Describe the morphology of the red blood cells.
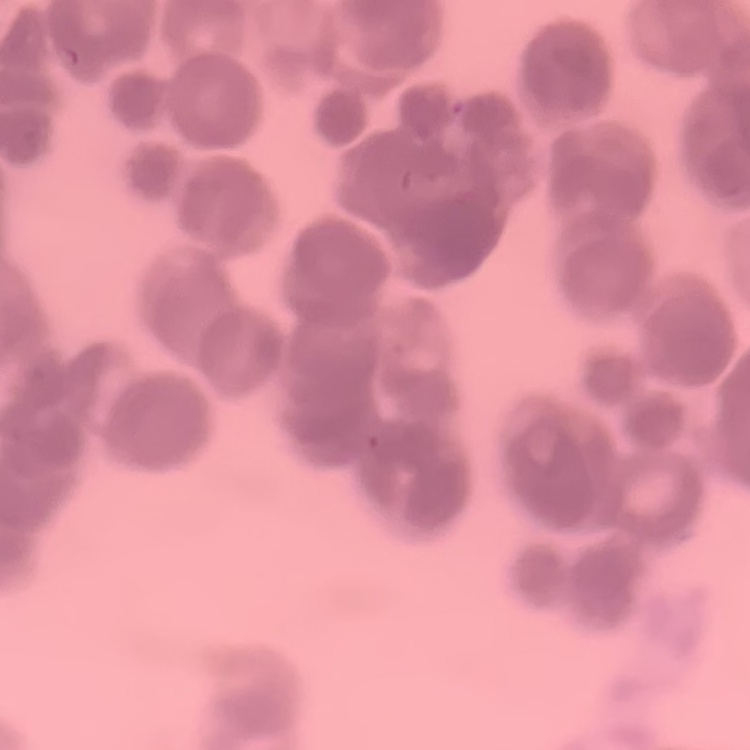

Rouleaux formation.

Thin peripheral smear. Square crop of a larger photomicrograph. Field's or Giemsa stain.